Name the parasite shown.
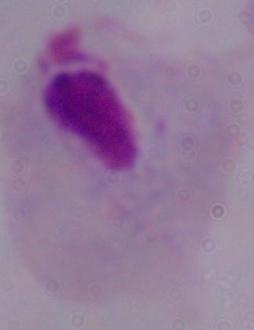
This is a trichomonad.

Summary:
  - Magnification: 1000x
  - Modality: photomicrograph